Classify this cell by malaria status.
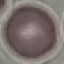
Uninfected.

Summary:
  - Image type: automatically extracted cell patch, resized to 64 × 64 pixels
  - Preparation: thin blood smear
  - Stain: Giemsa
  - Capture: smartphone camera at the microscope eyepiece